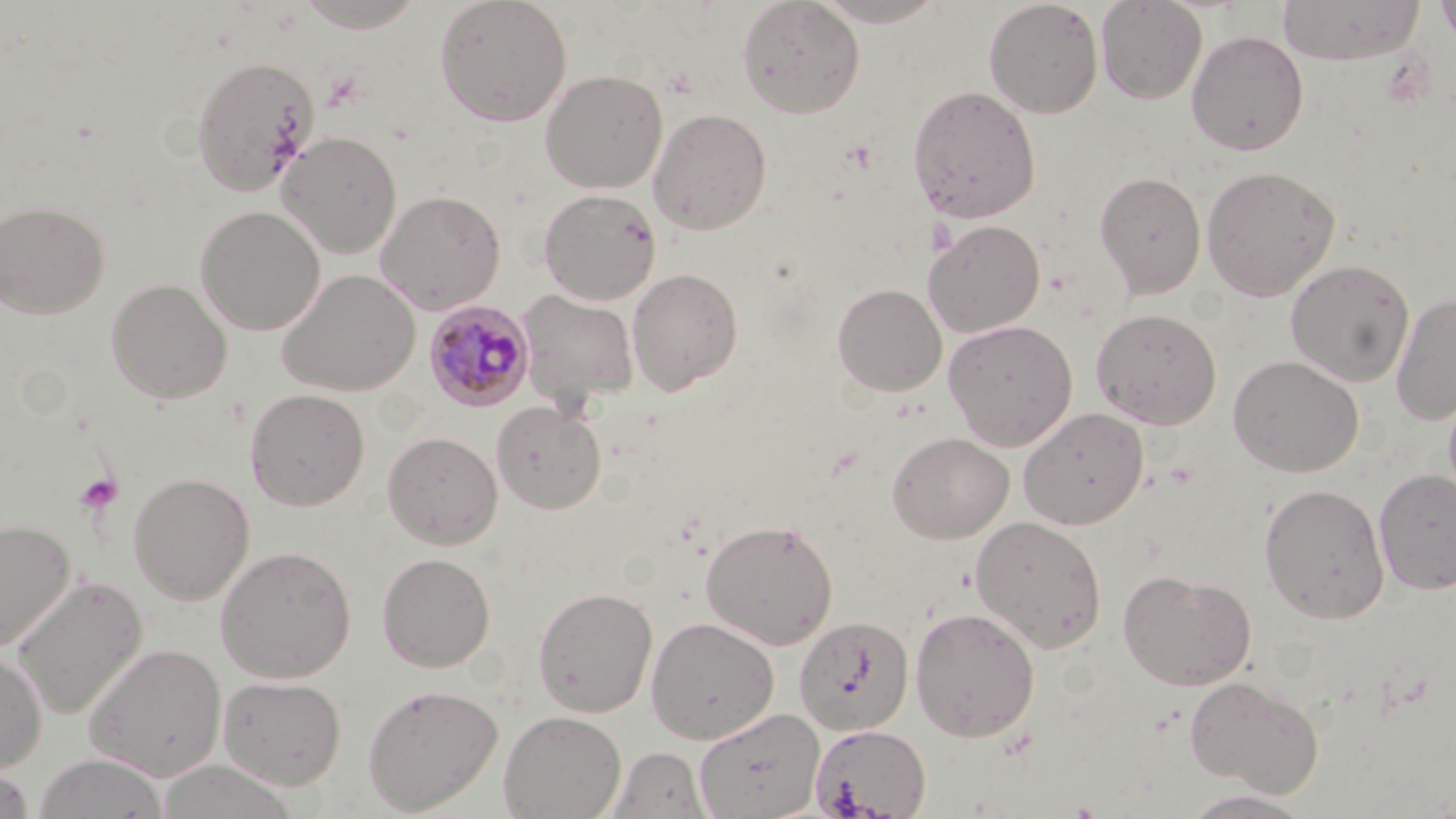

slide-level diagnosis = Plasmodium malariae
magnification = 1000x
Plasmodium malariae-infected red blood cell locations = approximate bounding boxes as (x1,y1)-(x2,y2) corner pairs in pixels: (424,301)-(535,412)
image size = 1456×819 pixels
modality = light microscopy
platelet locations = approximate bounding boxes as (x1,y1)-(x2,y2) corner pairs in pixels: (74,471)-(123,515)
uninfected red blood cell locations = approximate bounding boxes as (x1,y1)-(x2,y2) corner pairs in pixels: (294,0)-(428,32), (434,0)-(572,127), (736,0)-(865,118), (810,0)-(950,27), (983,0)-(1104,118), (1095,0)-(1207,104), (1278,0)-(1425,65), (1434,0)-(1456,48), (1187,30)-(1309,156), (190,56)-(320,195), (539,69)-(667,193), (907,84)-(1041,223), (648,107)-(772,234), (277,131)-(402,258), (1201,165)-(1340,301), (1095,170)-(1207,297), (538,188)-(661,305), (375,189)-(506,314), (0,199)-(110,319), (194,205)-(325,335), (923,219)-(1046,337), (1285,259)-(1415,386), (627,267)-(744,395), (276,268)-(421,396), (106,278)-(233,404), (832,283)-(947,396), (516,289)-(640,411), (1391,291)-(1456,425), (1091,307)-(1222,429), (943,318)-(1078,451), (1227,355)-(1364,477), (1442,381)-(1456,507), (244,388)-(370,510), (492,401)-(606,515), (1018,407)-(1150,529), (382,431)-(502,549), (887,431)-(1014,543), (1374,468)-(1456,595), (127,471)-(255,605), (1259,483)-(1390,624), (970,515)-(1108,653), (0,518)-(76,652), (700,518)-(839,650), (214,546)-(356,683), (376,552)-(496,672), (1118,569)-(1257,691), (11,575)-(148,720), (533,586)-(658,717), (910,606)-(1040,742), (645,616)-(779,744), (794,616)-(914,735), (84,643)-(226,781), (0,650)-(47,773), (217,674)-(347,790), (1184,675)-(1324,796), (362,683)-(503,814), (693,708)-(824,819), (498,710)-(626,819), (810,723)-(931,818), (608,746)-(712,819), (34,752)-(169,818), (0,762)-(36,819), (1178,788)-(1319,818)
preparation = thin blood smear
stain = May-Grünwald-Giemsa
field of view = one of a larger specimen